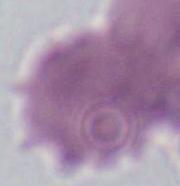
A red blood cell is shown. Captured at 1000x magnification. Micrograph.